State the preparation type.
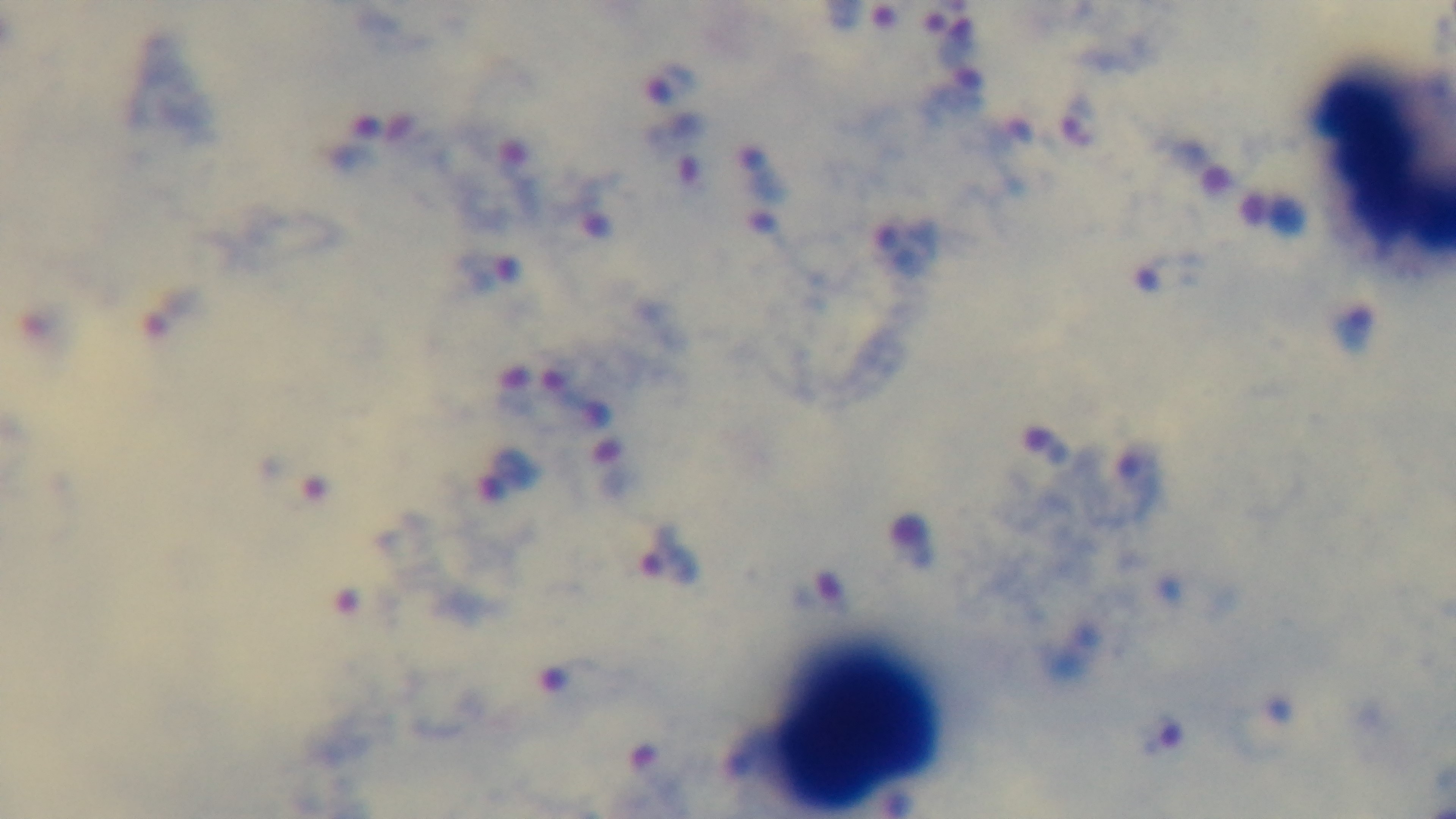

A thick smear.

Summary:
  - Field of view: one from the slide
  - Stain: Giemsa
  - Objective: 100x oil immersion
  - Malaria status: infected
  - Modality: light microscopy
  - Capture: mounted 4K digital camera